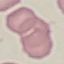

Malaria status: uninfected. Automatically extracted cell patch, resized to 64 × 64 pixels. Acquired by smartphone through the microscope eyepiece. Thin blood film. Giemsa stain.